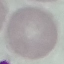

Malaria status: uninfected. Giemsa-stained preparation. Photographed with a smartphone camera at the microscope eyepiece. Thin smear of blood. Cell patch, automatically extracted from a larger field of view and resized to 64 × 64 pixels.